Assess this cell for malaria.
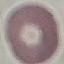

It is uninfected.

Summary:
  - Capture: smartphone through the microscope eyepiece
  - Stain: Giemsa
  - Preparation: thin smear
  - Image type: automatically extracted cell patch, resized to 64 × 64 pixels